Assess the morphology of the erythrocytes.
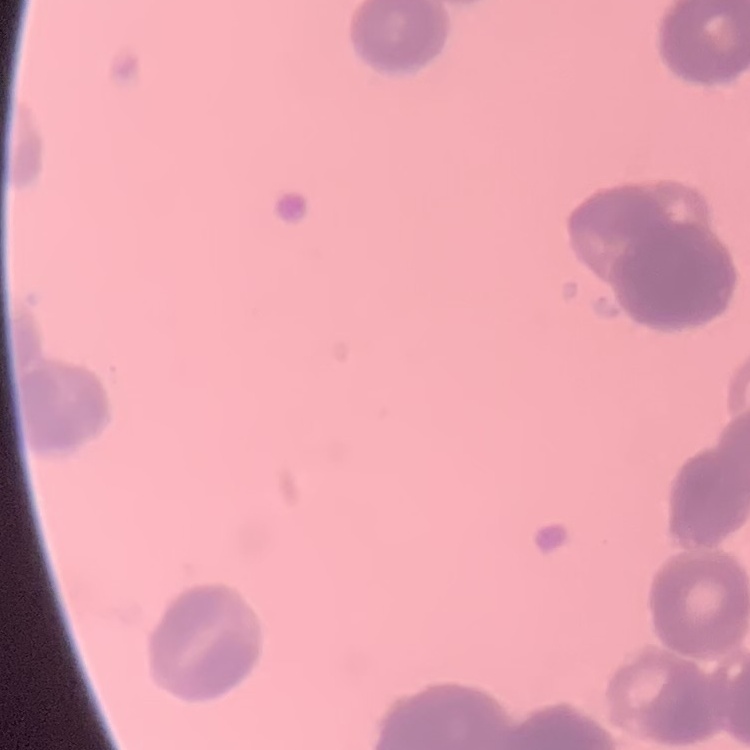

Rouleaux formation.

preparation = thin peripheral smear
stain = Field's or Giemsa
image type = one tile cut from a larger photomicrograph